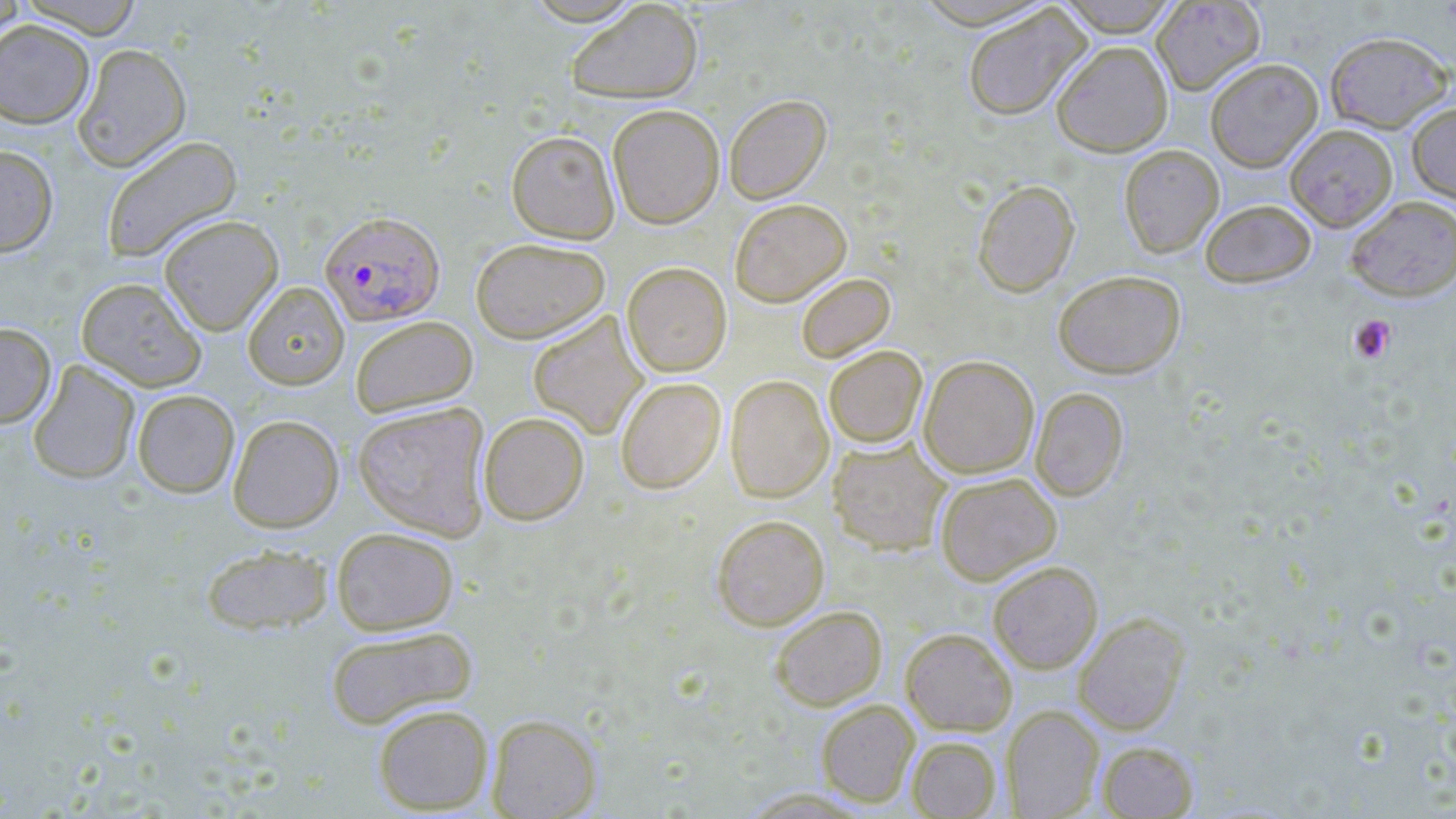

Summary:
  - Coordinate format: approximate bounding boxes as (x1,y1)-(x2,y2) corner pairs in pixels
  - Platelet locations: (1349,314)-(1398,364)
  - Uninfected red blood cell locations: (0,0)-(29,43), (17,0)-(145,38), (521,0)-(644,25), (565,0)-(703,104), (908,0)-(1057,29), (1054,0)-(1182,37), (1151,0)-(1265,95), (962,6)-(1091,121), (0,19)-(95,129), (1324,30)-(1454,133), (1051,41)-(1173,157), (73,42)-(191,171), (1204,58)-(1323,172), (724,93)-(831,203), (607,103)-(724,228), (1407,103)-(1456,205), (1285,124)-(1398,231), (506,130)-(620,244), (100,134)-(242,263), (0,144)-(59,256), (1118,144)-(1224,257), (972,179)-(1080,297), (1345,195)-(1456,301), (729,198)-(851,306), (1200,199)-(1316,288), (158,214)-(284,335), (470,237)-(610,343), (622,262)-(732,377), (1053,270)-(1186,378), (796,273)-(895,362), (76,277)-(206,392), (243,282)-(349,390), (528,311)-(648,440), (350,315)-(478,417), (0,322)-(56,428), (823,345)-(927,448), (919,354)-(1039,478), (28,360)-(140,484), (724,374)-(834,502), (615,376)-(726,494), (1030,387)-(1128,501), (132,389)-(240,497), (352,401)-(492,540), (478,411)-(589,526), (227,414)-(344,532), (828,438)-(951,556), (935,472)-(1062,585), (711,514)-(829,630), (331,526)-(459,635), (201,543)-(333,636), (988,561)-(1103,673), (770,605)-(887,710), (1073,613)-(1190,735), (325,625)-(478,729), (900,627)-(1017,735), (816,699)-(919,807), (373,704)-(493,814), (1003,706)-(1103,818), (487,714)-(602,818), (906,736)-(1001,818), (1096,740)-(1199,818)
  - Plasmodium falciparum-infected red blood cell locations: (319,211)-(446,326)
  - Slide-level diagnosis: Plasmodium falciparum
  - Field of view: single
  - Modality: light microscopy
  - Stain: May-Grünwald-Giemsa
  - Preparation: thin blood smear
  - Magnification: 1000x
  - Image size: 1456×819 pixels